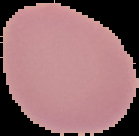

Summary:
  - Result: negative for Plasmodium parasites
  - Preparation: thin blood smear
  - Image size: 139×136 pixels
  - Image type: segmented cell region on a black background